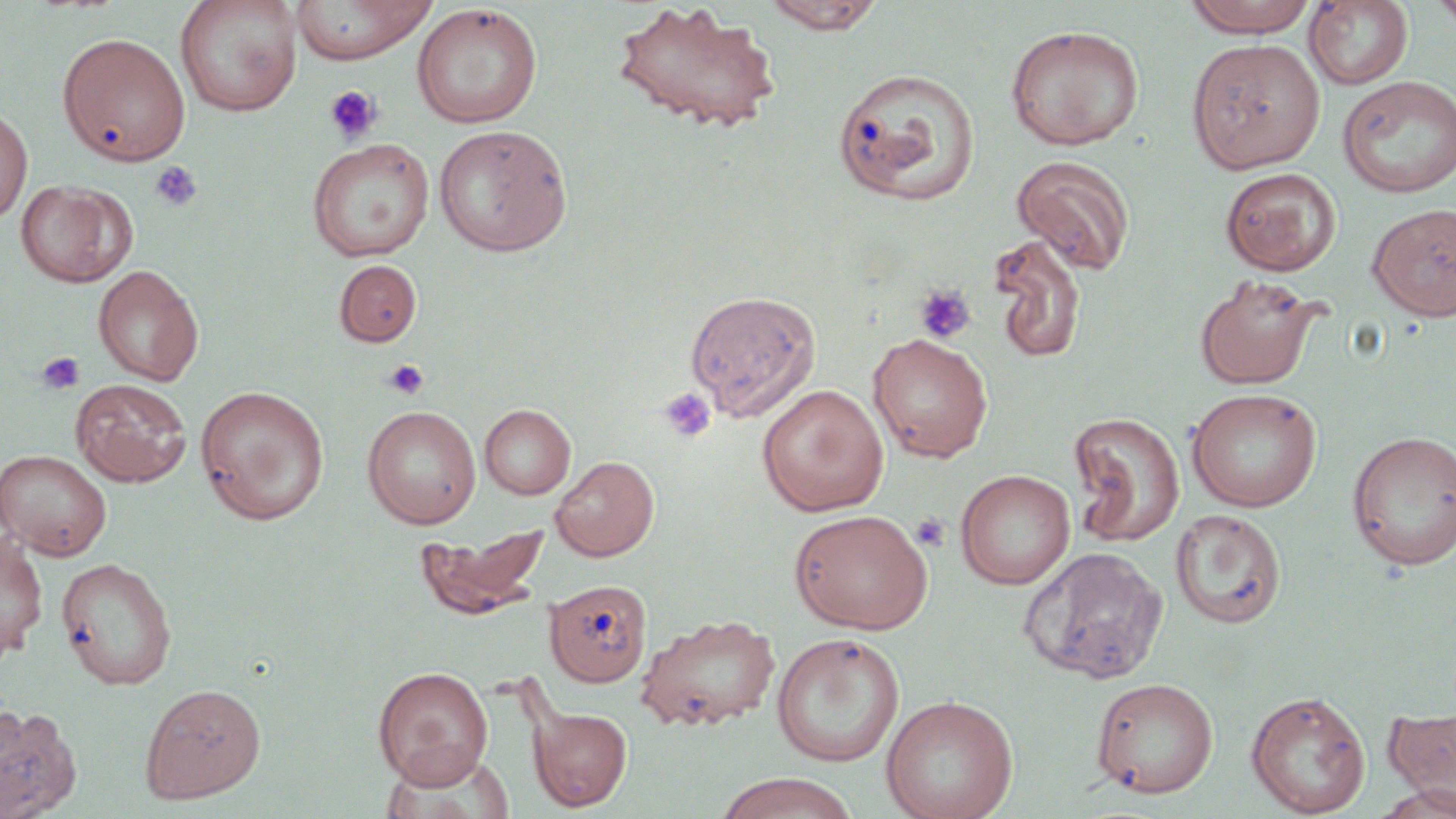 Approximate bounding boxes as (x1,y1)-(x2,y2) corner pairs in pixels. Uninfected red blood cell locations: (175,0)-(303,117), (760,0)-(887,33), (1182,0)-(1319,37), (290,1)-(438,64), (611,1)-(780,134), (1304,1)-(1414,91), (1431,1)-(1456,36), (411,3)-(543,129), (1005,24)-(1146,150), (58,31)-(192,168), (1187,39)-(1325,173), (833,67)-(981,207), (1337,76)-(1455,198), (0,106)-(33,224), (434,124)-(573,257), (306,138)-(434,262), (1011,154)-(1136,274), (1220,166)-(1342,276), (15,179)-(137,287), (1367,203)-(1456,321), (987,232)-(1088,364), (334,259)-(422,347), (93,265)-(203,386), (1194,274)-(1324,390), (684,290)-(821,422), (867,332)-(993,462), (71,379)-(192,487), (756,384)-(888,516), (194,385)-(330,525), (1186,388)-(1322,512), (479,404)-(575,499), (362,405)-(481,528), (1068,412)-(1185,547), (1347,430)-(1456,570), (0,449)-(112,561), (550,456)-(659,561), (955,469)-(1075,590), (787,508)-(933,634), (1170,509)-(1287,629), (414,522)-(549,619), (0,532)-(49,657), (1018,546)-(1168,684), (56,557)-(177,689), (545,580)-(652,686), (635,612)-(781,732), (771,633)-(904,767), (373,666)-(493,787), (1090,677)-(1219,798), (139,682)-(266,803), (1245,690)-(1370,817), (880,694)-(1018,819), (0,704)-(82,819), (528,706)-(632,811), (1384,706)-(1456,809), (376,748)-(516,819), (711,772)-(861,819). Platelet locations: (324,85)-(383,145), (149,161)-(201,211), (913,283)-(977,344), (37,351)-(84,396), (384,360)-(430,400), (660,387)-(717,443), (911,514)-(951,552). Slide-level diagnosis: negative for blood parasites. Thin blood smear. One field of a larger specimen. Image is 1456×819 pixels. May-Grünwald-Giemsa stain. Light microscopy. 1000x magnification.